State which parasite is depicted.
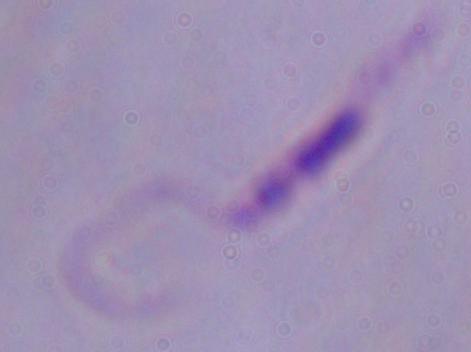
Leishmania.

Micrograph. 1000x magnification.